Locate every blood parasite and identify its species.
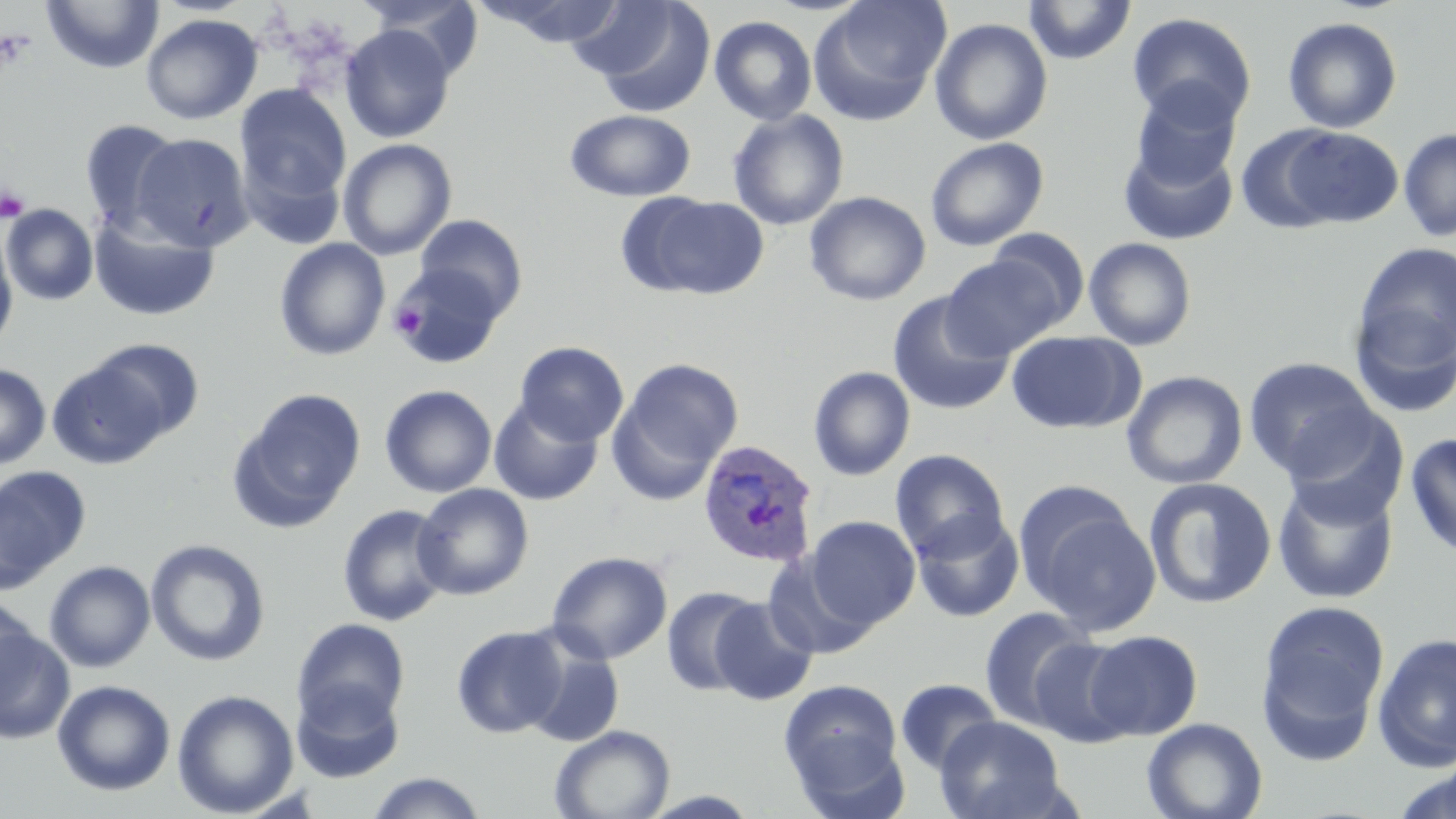

Approximate bounding boxes as [x1, y1, x2, y2] in pixels.
Plasmodium ovale-infected red blood cells: [696, 439, 820, 568].
No Plasmodium falciparum, Plasmodium malariae, Plasmodium vivax, Babesia divergens, or Trypanosoma brucei observed.

slide_level_diagnosis: Plasmodium ovale
platelet_locations: 'approximate bounding boxes as [x1, y1, x2, y2] in pixels: [0, 186, 29, 221], [390, 302, 429, 340]'
uninfected_red_blood_cell_locations: 'approximate bounding boxes as [x1, y1, x2, y2] in pixels: [41, 0, 164, 74], [357, 0, 486, 81], [474, 0, 630, 48], [584, 0, 716, 117], [809, 0, 950, 123], [1022, 0, 1138, 65], [1127, 12, 1257, 130], [140, 13, 263, 125], [709, 16, 817, 126], [1282, 17, 1402, 134], [930, 18, 1053, 146], [340, 24, 456, 143], [1130, 83, 1241, 191], [235, 84, 352, 210], [565, 109, 696, 201], [727, 109, 849, 230], [79, 119, 184, 233], [1235, 126, 1345, 233], [1280, 127, 1404, 229], [1398, 127, 1456, 242], [132, 133, 254, 252], [925, 137, 1048, 251], [338, 138, 457, 260], [1118, 139, 1238, 246], [804, 191, 932, 306], [640, 195, 769, 298], [1, 204, 98, 305], [89, 213, 219, 322], [415, 214, 527, 320], [986, 227, 1090, 330], [0, 231, 18, 353], [1083, 237, 1197, 351], [274, 238, 390, 361], [1350, 240, 1455, 378], [939, 254, 1065, 360], [389, 263, 505, 368], [887, 291, 1015, 415], [1346, 297, 1456, 419], [1006, 331, 1142, 434], [83, 338, 206, 444], [515, 341, 629, 445], [47, 354, 174, 469], [1243, 356, 1380, 479], [613, 358, 743, 493], [0, 364, 51, 469], [808, 366, 916, 481], [1122, 371, 1247, 489], [379, 384, 497, 498], [230, 388, 366, 530], [489, 397, 604, 507], [1278, 406, 1408, 530], [1404, 433, 1456, 561], [890, 449, 1010, 562], [0, 466, 89, 592], [1272, 476, 1399, 604], [1143, 478, 1277, 609], [412, 483, 534, 600], [1021, 494, 1161, 634], [336, 503, 453, 627], [910, 510, 1025, 623], [805, 516, 920, 628], [145, 539, 270, 666], [763, 549, 880, 660], [547, 550, 672, 665], [44, 561, 155, 672], [661, 585, 766, 697], [0, 595, 38, 707], [709, 596, 818, 705], [1256, 600, 1390, 753], [978, 605, 1098, 731], [292, 618, 410, 731], [451, 625, 568, 738], [0, 626, 75, 744], [1081, 630, 1203, 740], [1372, 632, 1456, 771], [1029, 637, 1137, 748], [521, 638, 624, 747], [894, 678, 1003, 776], [779, 679, 907, 808], [52, 680, 176, 796], [291, 680, 405, 783], [172, 689, 299, 817], [935, 716, 1068, 819], [1142, 717, 1268, 819], [549, 725, 675, 819], [1392, 763, 1456, 819], [361, 772, 490, 818]'
magnification: 1000x
image_size: 1456×819 pixels
modality: optical microscopy
preparation: thin blood smear
stain: May-Grünwald-Giemsa
field_of_view: single